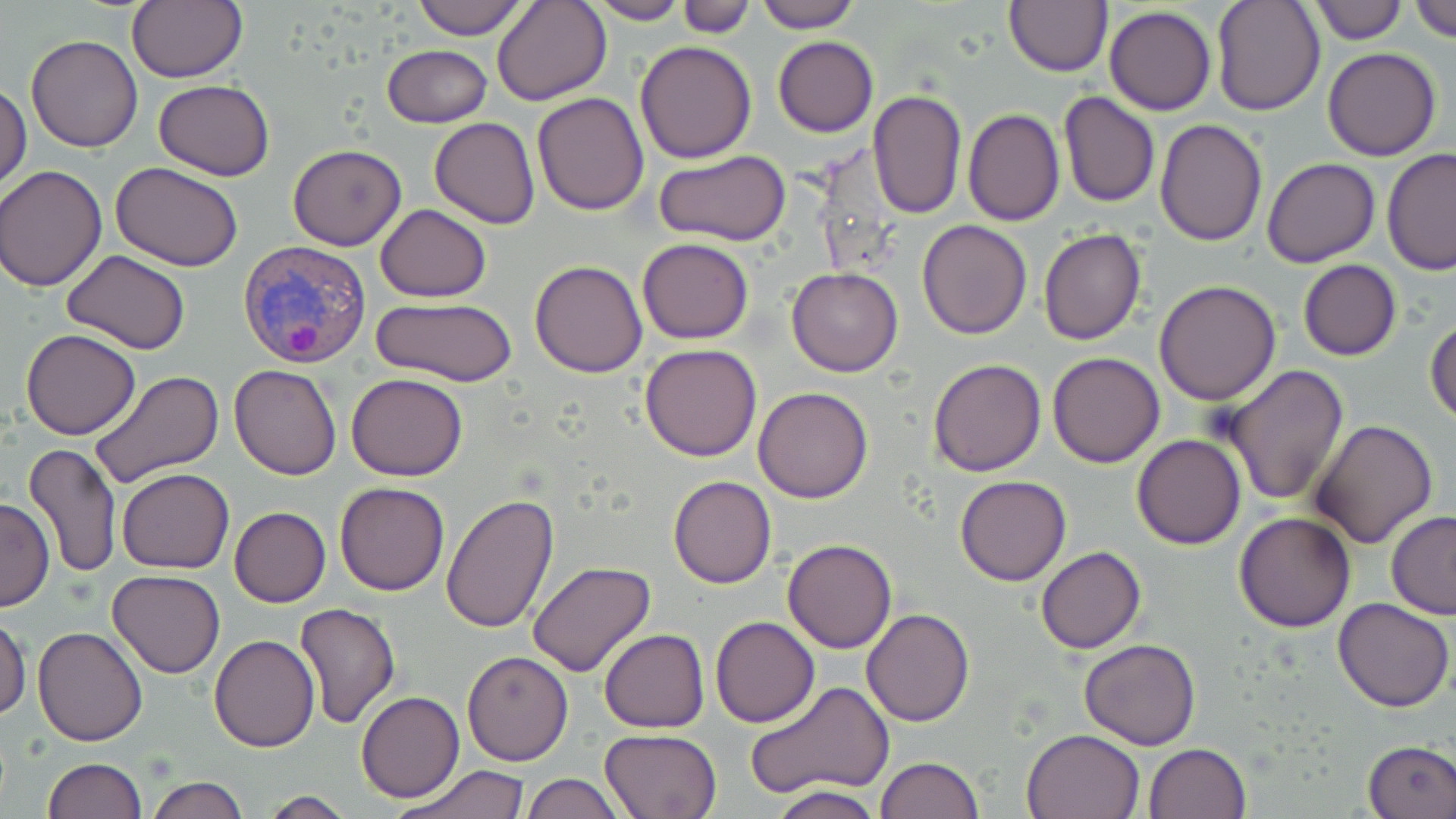
{
  "slide_level_diagnosis": "Plasmodium vivax",
  "magnification": "1000x",
  "plasmodium_vivax_infected_red_blood_cell_locations": "approximate bounding boxes as [x1, y1, x2, y2] in pixels: [239, 240, 371, 369]",
  "stain": "May-Grünwald-Giemsa",
  "uninfected_red_blood_cell_locations": "approximate bounding boxes as [x1, y1, x2, y2] in pixels: [126, 0, 248, 85], [411, 0, 530, 39], [493, 0, 612, 105], [752, 0, 861, 33], [1211, 0, 1325, 116], [1410, 0, 1456, 41], [584, 1, 690, 24], [676, 1, 755, 38], [1005, 1, 1113, 76], [1309, 1, 1407, 46], [1105, 6, 1217, 115], [26, 34, 143, 152], [773, 36, 878, 137], [635, 42, 756, 164], [384, 45, 492, 128], [1322, 47, 1443, 161], [152, 80, 276, 181], [1, 82, 31, 193], [867, 90, 966, 219], [532, 92, 650, 215], [1057, 92, 1160, 207], [963, 108, 1064, 226], [429, 117, 539, 229], [1154, 119, 1267, 247], [288, 144, 406, 250], [1381, 149, 1456, 275], [655, 150, 792, 247], [1262, 158, 1381, 268], [111, 162, 243, 271], [1, 166, 107, 290], [376, 203, 491, 302], [917, 219, 1033, 339], [1039, 227, 1146, 345], [637, 238, 754, 345], [63, 249, 190, 353], [530, 260, 647, 378], [1297, 260, 1402, 361], [787, 267, 903, 376], [1153, 279, 1282, 405], [368, 299, 523, 387], [1426, 317, 1456, 426], [21, 328, 141, 440], [639, 343, 763, 462], [1047, 351, 1164, 467], [928, 358, 1046, 476], [230, 364, 342, 480], [1222, 365, 1349, 507], [89, 370, 225, 490], [346, 373, 467, 481], [752, 386, 874, 503], [1309, 419, 1438, 550], [1131, 434, 1246, 549], [24, 444, 123, 578], [118, 469, 234, 573], [668, 475, 777, 589], [955, 475, 1072, 586], [334, 481, 451, 596], [0, 495, 54, 612], [441, 495, 560, 634], [229, 506, 331, 607], [1234, 511, 1357, 632], [1386, 511, 1456, 620], [784, 537, 897, 653], [1036, 546, 1146, 654], [526, 560, 656, 677], [106, 569, 228, 678], [1332, 596, 1454, 712], [296, 601, 400, 728], [862, 609, 974, 728], [0, 615, 30, 722], [711, 616, 819, 728], [32, 626, 149, 746], [600, 629, 709, 732], [210, 634, 319, 752], [1079, 639, 1201, 748], [461, 649, 574, 765], [745, 681, 894, 801], [356, 691, 464, 803], [600, 727, 722, 819], [1021, 728, 1144, 818], [1362, 739, 1456, 818], [1144, 743, 1251, 819], [876, 757, 984, 819], [43, 758, 145, 819], [394, 763, 532, 818], [521, 774, 627, 818], [147, 776, 249, 819], [768, 786, 885, 819], [258, 791, 355, 818]",
  "modality": "light microscopy",
  "image_size": "1456×819 pixels",
  "field_of_view": "one of a larger specimen",
  "preparation": "thin blood film"
}